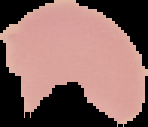
Cell region segmented out of the field of view; the surrounding area is masked to black. Image is 148×127 pixels. Malaria status: uninfected. From a thin blood smear.